Report the malaria status of this cell.
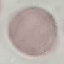
It is uninfected.

stain = Giemsa
image type = automatically extracted cell patch, resized to 64 × 64 pixels
capture = smartphone camera at the microscope eyepiece
preparation = thin blood smear